Classify this cell by malaria status.
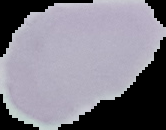
It is uninfected.

Summary:
  - Preparation: thin blood smear
  - Image type: cell region segmented out of the field of view; surrounding area masked to black
  - Image size: 166×130 pixels